Point out each Plasmodium parasite.
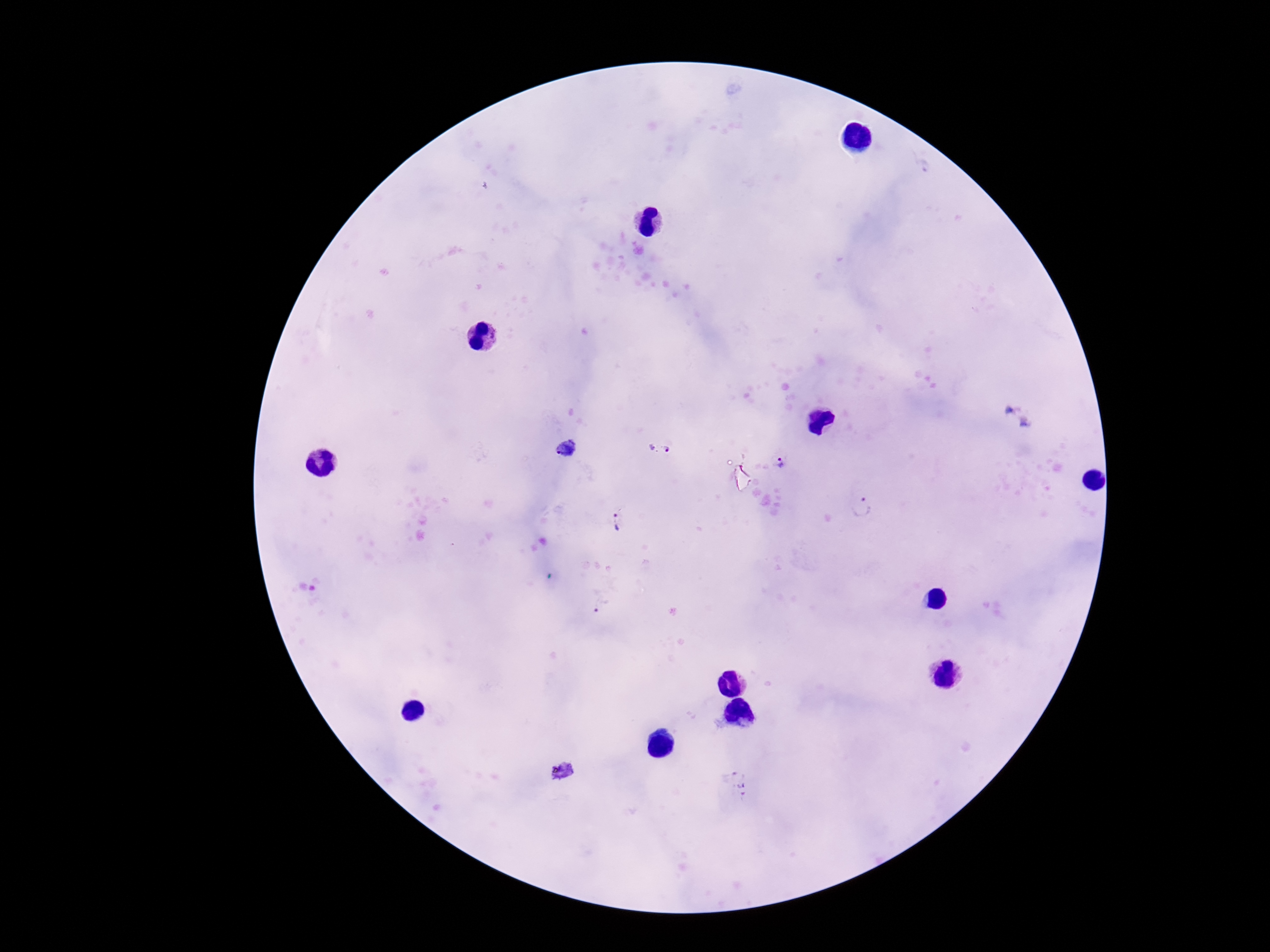
Approximate centers as [x, y] in pixels.
Plasmodium parasites: [652, 447], [668, 448], [568, 449], [780, 463], [862, 510], [618, 521], [728, 772], [744, 788].

{
  "stain": "Giemsa",
  "patient_malaria_status": "infected",
  "image_size": "1270×952 pixels",
  "magnification": "100x",
  "preparation": "thick peripheral-blood smear",
  "field_of_view": "single",
  "capture": "smartphone camera through the microscope eyepiece"
}